Locate every blood parasite and identify its species.
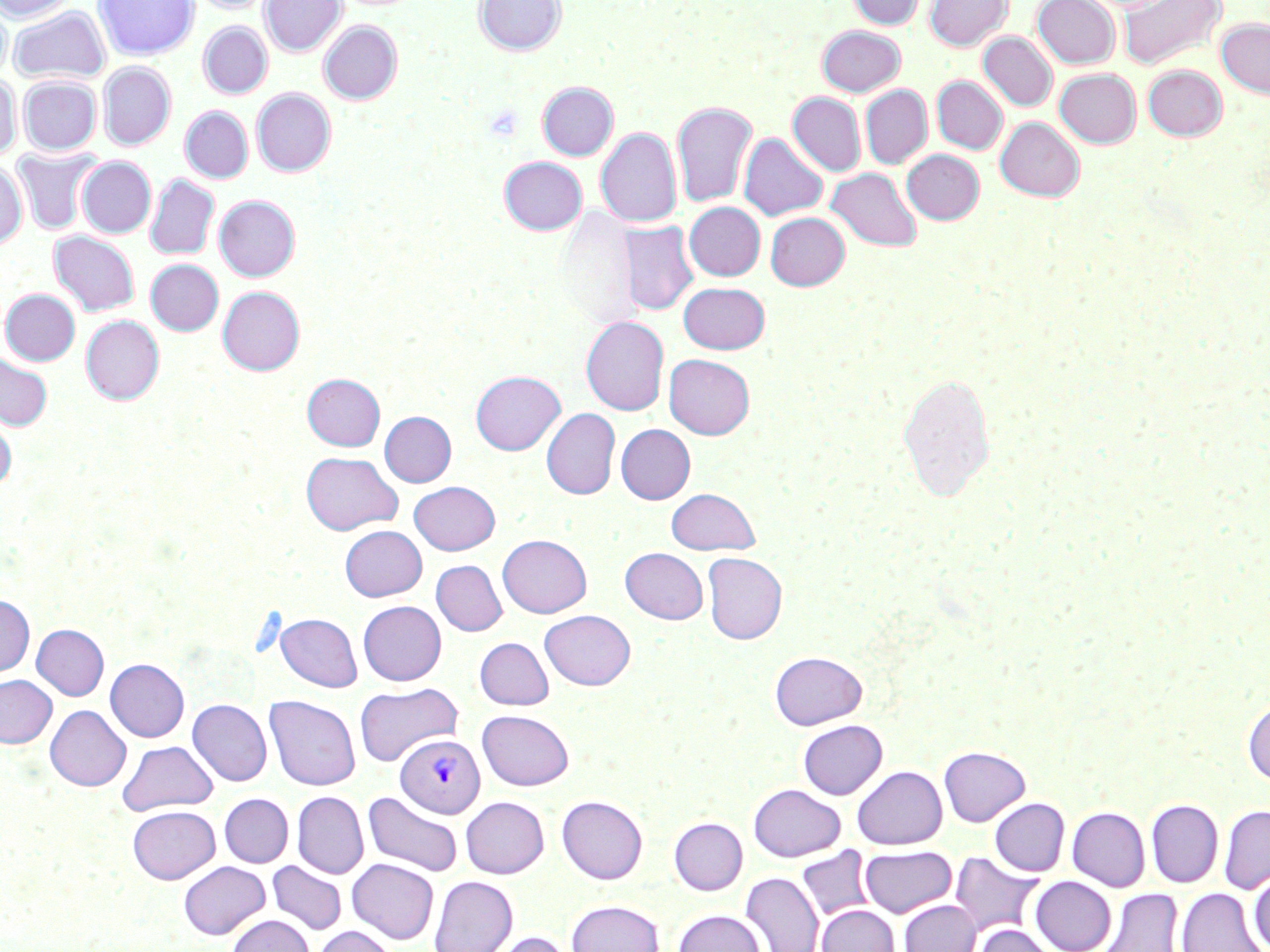
Approximate bounding boxes as (x1,y1)-(x2,y2) corner pairs in pixels.
Plasmodium vivax-infected red blood cells: (395,734)-(485,819).
No Plasmodium falciparum, Plasmodium ovale, Plasmodium malariae, Babesia divergens, or Trypanosoma brucei observed.

Summary:
  - Uninfected red blood cell locations: (0,0)-(78,23), (94,0)-(198,60), (191,0)-(273,14), (260,0)-(346,58), (474,0)-(566,56), (848,0)-(926,30), (925,0)-(1012,51), (1032,0)-(1120,69), (1118,0)-(1225,71), (0,4)-(11,80), (9,6)-(110,85), (1216,19)-(1270,99), (319,21)-(402,104), (198,22)-(272,98), (817,26)-(906,96), (978,32)-(1057,111), (98,61)-(175,150), (1142,65)-(1227,141), (1054,69)-(1141,148), (0,74)-(21,160), (18,76)-(100,155), (932,76)-(1007,154), (537,82)-(618,160), (861,85)-(932,168), (251,89)-(336,176), (788,92)-(865,176), (672,101)-(758,208), (180,107)-(253,183), (995,117)-(1085,201), (596,127)-(681,228), (739,132)-(828,221), (13,148)-(101,234), (901,149)-(984,224), (499,156)-(587,234), (77,157)-(155,237), (0,160)-(28,249), (827,167)-(922,252), (145,174)-(219,260), (214,195)-(300,281), (684,202)-(765,281), (557,208)-(641,328), (765,212)-(849,290), (618,221)-(699,316), (49,231)-(139,316), (146,260)-(223,335), (678,282)-(771,354), (218,286)-(305,375), (1,289)-(80,366), (81,315)-(164,404), (581,316)-(669,415), (0,353)-(52,431), (664,354)-(755,439), (471,370)-(565,455), (897,372)-(996,502), (302,374)-(385,450), (542,409)-(620,499), (0,410)-(16,492), (380,411)-(456,487), (615,424)-(695,504), (300,451)-(402,535), (409,481)-(500,555), (665,488)-(760,555), (340,525)-(427,601), (497,534)-(591,618), (621,547)-(708,624), (702,553)-(787,644), (431,560)-(507,636), (0,595)-(34,677), (358,600)-(446,685), (539,610)-(636,690), (275,613)-(362,692), (31,624)-(109,700), (475,637)-(553,709), (770,651)-(867,730), (105,659)-(189,742), (0,674)-(56,748), (355,683)-(462,766), (265,695)-(360,790), (1243,698)-(1270,786), (187,699)-(272,786), (45,705)-(131,791), (477,710)-(574,790), (798,719)-(888,800), (118,740)-(218,816), (938,746)-(1030,826), (852,766)-(947,849), (748,783)-(846,861), (292,791)-(369,879), (363,791)-(463,877), (220,793)-(293,867), (557,795)-(648,883), (460,796)-(549,878), (990,798)-(1069,876), (1146,799)-(1223,888), (1219,805)-(1270,894), (127,806)-(220,883), (1068,807)-(1150,891), (669,817)-(747,894), (859,846)-(956,918), (796,847)-(875,923), (950,853)-(1044,937), (347,858)-(439,944), (178,861)-(270,939), (267,861)-(347,935), (1250,871)-(1270,951), (740,872)-(823,952), (429,876)-(517,952), (1031,876)-(1116,952), (1178,887)-(1267,952), (1100,889)-(1184,952), (566,899)-(664,952), (899,900)-(980,952), (818,904)-(899,952), (673,909)-(765,952), (227,914)-(314,952), (974,924)-(1056,952), (313,926)-(398,952), (488,930)-(575,952)
  - Slide-level diagnosis: Plasmodium vivax
  - Preparation: thin blood film
  - Magnification: 1000x
  - Image size: 1270×952 pixels
  - Modality: light microscopy
  - Stain: May-Grünwald-Giemsa
  - Field of view: single